Classify this cell by malaria status.
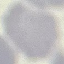

It is uninfected.

Automatically extracted cell patch, resized to 64 × 64 pixels. Thin blood film. Photographed with a smartphone camera at the microscope eyepiece. Giemsa stain.